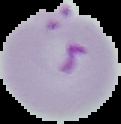
preparation: thin blood smear
image_type: segmented cell region with the area outside set to black
image_size: 121×124 pixels
malaria_status: parasitized